Name the parasite shown.
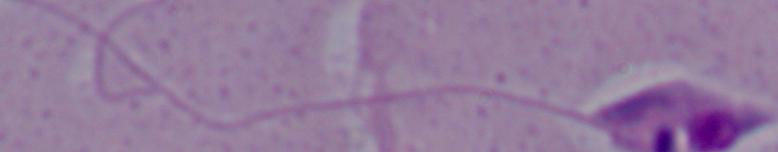

Leishmania.

1000x magnification. Photomicrograph.